Report the malaria status.
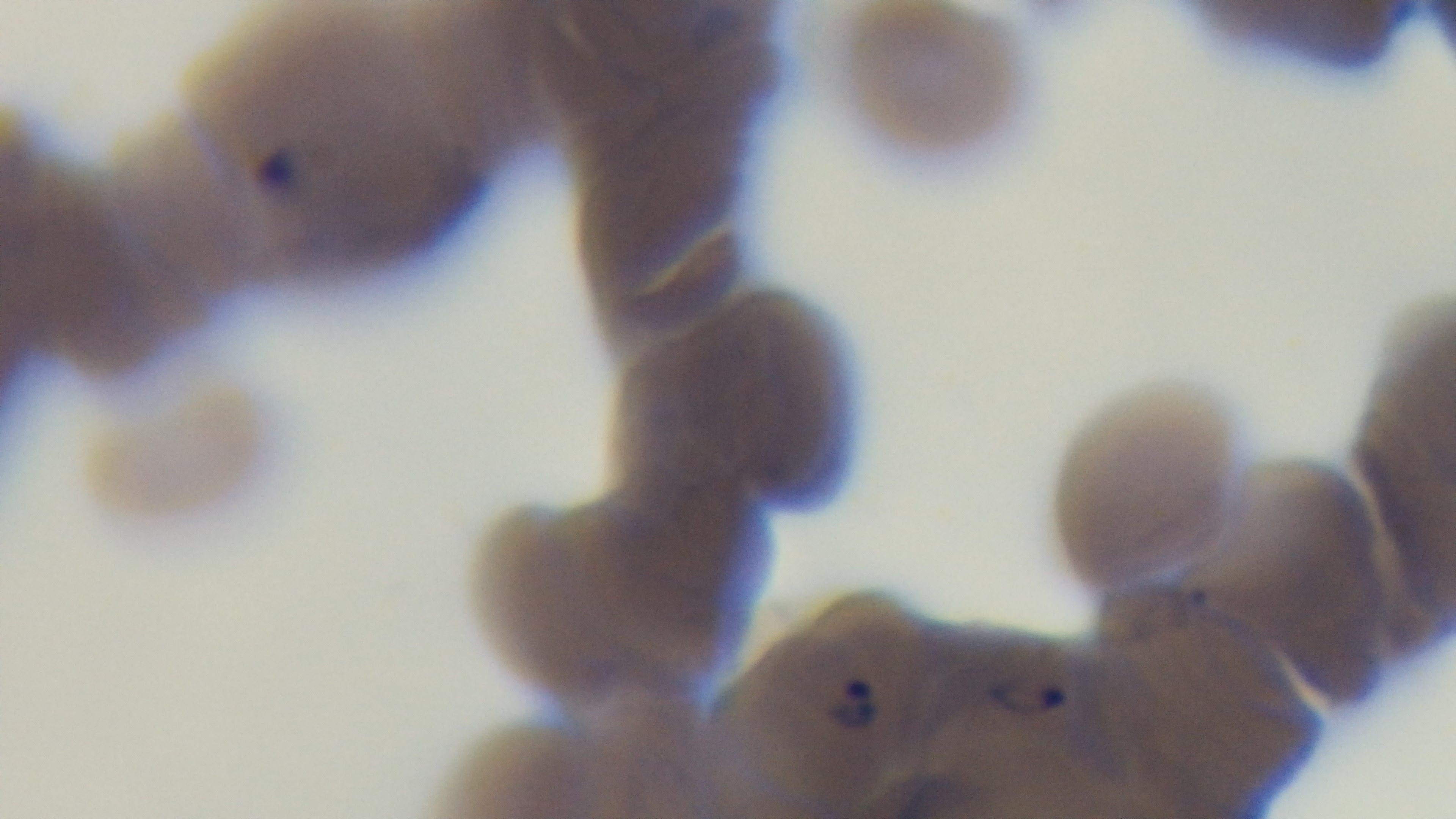

Positive.

One field from the slide. 100x oil-immersion objective. Mounted 4K digital camera. Giemsa-stained. Preparation: thin smear. Light microscopy.